Report the malaria status of this cell.
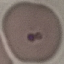

It is uninfected.

Acquired by smartphone through the microscope eyepiece. Giemsa-stained preparation. Cell patch, automatically extracted from a larger field of view and resized to 64 × 64 pixels. Thin blood film.